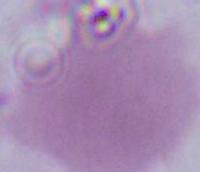

magnification: 1000x
modality: photomicrograph
identification: red blood cell